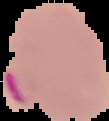 Cell region segmented out of the field of view; the surrounding area is masked to black. Image is 109×121 pixels. From a thin blood film. Result: Plasmodium parasites detected.